Assess this cell for malaria.
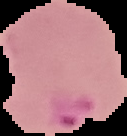
It is parasitized.

Summary:
  - Image size: 127×136 pixels
  - Preparation: thin blood film
  - Image type: cell region segmented out of the field of view; surrounding area masked to black